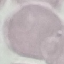 Malaria status: uninfected. Acquired by smartphone through the microscope eyepiece. Thin smear of blood. Giemsa stain. Automatically extracted cell patch, resized to 64 × 64 pixels.